Identify the blood parasite species.
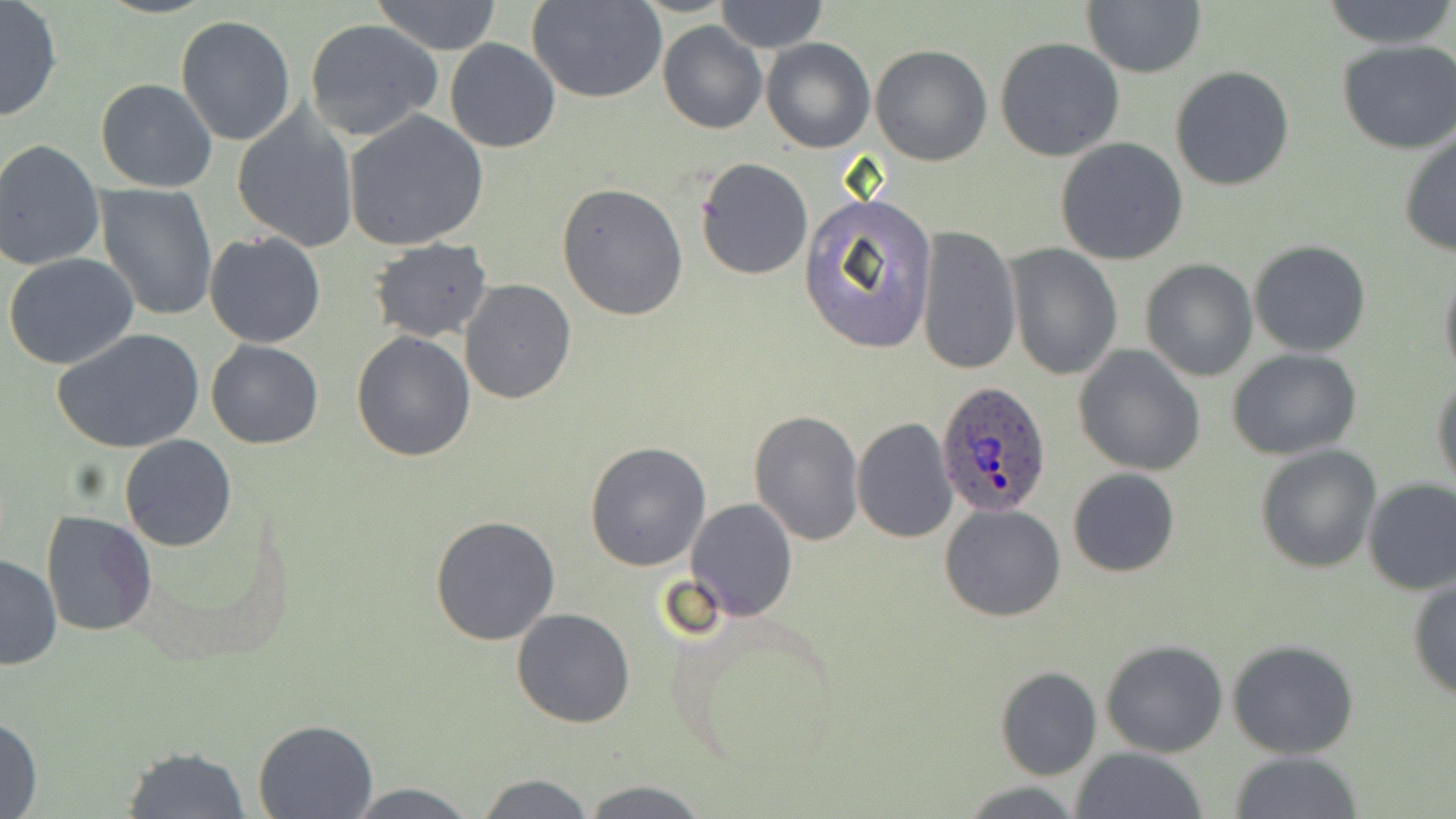
Plasmodium ovale.

modality = light microscopy
stain = May-Grünwald-Giemsa
preparation = thin blood film
uninfected red blood cell locations = approximate bounding boxes as [x1, y1, x2, y2] in pixels: [369, 0, 504, 54], [530, 0, 667, 104], [715, 0, 827, 53], [1321, 0, 1456, 51], [0, 1, 63, 123], [1082, 2, 1206, 79], [175, 16, 296, 146], [304, 19, 443, 141], [657, 22, 767, 134], [995, 37, 1125, 161], [761, 38, 874, 153], [444, 39, 561, 153], [1337, 40, 1456, 153], [871, 44, 994, 167], [1171, 65, 1294, 191], [95, 79, 218, 192], [232, 109, 359, 251], [345, 110, 489, 251], [1398, 130, 1456, 258], [1055, 138, 1189, 266], [0, 140, 105, 271], [695, 156, 812, 281], [557, 182, 689, 322], [95, 184, 217, 321], [801, 193, 938, 350], [917, 225, 1021, 376], [205, 231, 325, 348], [368, 237, 493, 343], [1248, 239, 1373, 357], [1005, 243, 1122, 381], [4, 254, 140, 371], [1140, 258, 1258, 382], [1439, 265, 1456, 381], [459, 280, 576, 405], [52, 328, 205, 453], [351, 332, 476, 461], [206, 341, 323, 449], [1072, 345, 1207, 477], [1228, 349, 1362, 459], [1431, 372, 1456, 493], [751, 409, 864, 544], [851, 416, 958, 542], [119, 435, 236, 551], [585, 442, 712, 570], [1254, 444, 1381, 572], [1068, 468, 1181, 578], [1362, 477, 1456, 595], [685, 498, 798, 620], [940, 503, 1067, 621], [40, 510, 158, 637], [430, 514, 561, 647], [1, 553, 62, 670], [1408, 577, 1456, 702], [512, 608, 636, 729], [1099, 638, 1228, 757], [1227, 639, 1359, 759], [995, 666, 1102, 780], [1, 712, 43, 819], [252, 718, 379, 819], [118, 744, 253, 818], [1072, 746, 1209, 819], [1228, 751, 1364, 819], [472, 771, 596, 817], [580, 780, 709, 817], [958, 780, 1085, 817], [344, 783, 480, 817]
image size = 1456×819 pixels
Plasmodium ovale-infected red blood cell locations = approximate bounding boxes as [x1, y1, x2, y2] in pixels: [935, 383, 1052, 517]
field of view = one of a larger specimen
magnification = 1000x